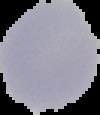

image size = 100×115 pixels
image type = segmented cell region with the area outside set to black
result = no malaria parasites seen
preparation = thin blood smear